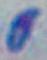
Summary:
  - Identification: Toxoplasma gondii
  - Modality: photomicrograph
  - Magnification: 1000x